Assess this cell for malaria.
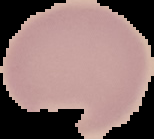
It is uninfected.

image size = 154×139 pixels
image type = segmented cell region on a black background
preparation = thin blood smear